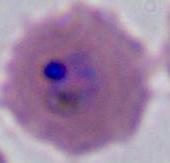

Summary:
  - Modality: micrograph
  - Identification: Plasmodium
  - Magnification: 400x or 1000x